Locate every Plasmodium parasite.
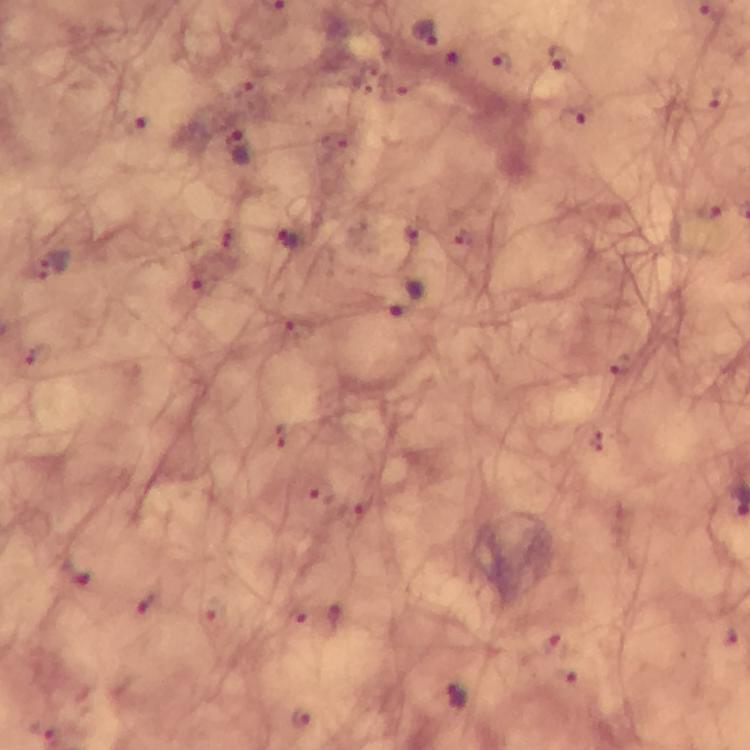
Approximate centers as (x, y) in pixels.
Plasmodium parasites: (424, 32), (558, 56), (500, 62), (719, 99), (571, 119), (238, 150), (288, 241), (57, 263), (404, 296), (457, 697), (300, 716).

Smartphone photograph taken through a microscope. A crop from one field of view. Image is 750×750 pixels. From a malaria diagnostic workup. Immersion oil applied. Thick blood film. 100x magnification. Giemsa-stained preparation.